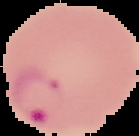

Cell region segmented out of the field of view; the surrounding area is masked to black. From a thin blood film. Result: Plasmodium parasites detected. Image is 139×136 pixels.